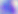
Summary:
  - Identification: Toxoplasma gondii
  - Magnification: 400x
  - Modality: photomicrograph